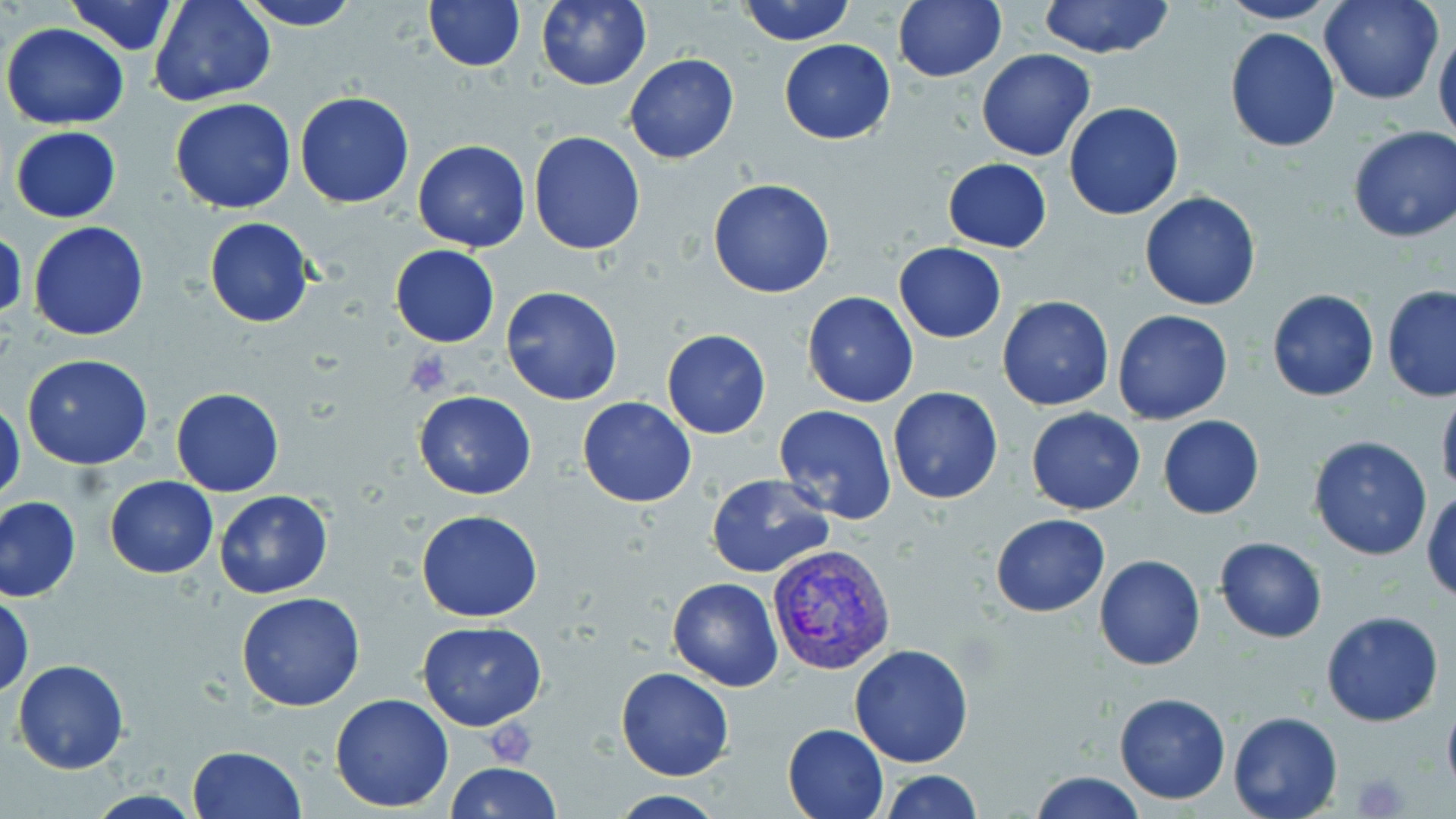

Approximate bounding boxes as [x1, y1, x2, y2] in pixels. Platelet locations: [402, 349, 454, 398], [483, 718, 540, 765], [1353, 772, 1410, 818]. Plasmodium vivax-infected red blood cell locations: [767, 543, 897, 676]. Uninfected red blood cell locations: [64, 0, 182, 55], [149, 0, 275, 107], [236, 0, 362, 31], [424, 0, 525, 71], [535, 0, 651, 90], [738, 0, 856, 45], [894, 0, 1007, 84], [1038, 0, 1175, 58], [1319, 0, 1442, 105], [1216, 1, 1342, 26], [3, 23, 129, 129], [1224, 27, 1340, 153], [1433, 27, 1456, 155], [778, 39, 896, 145], [976, 48, 1096, 161], [624, 52, 739, 165], [1005, 71, 1141, 189], [295, 92, 414, 209], [169, 97, 297, 214], [1064, 101, 1185, 220], [10, 126, 122, 222], [1347, 127, 1456, 243], [529, 131, 645, 255], [412, 139, 531, 252], [942, 159, 1053, 252], [707, 177, 837, 299], [1139, 191, 1262, 311], [204, 216, 314, 328], [27, 220, 150, 341], [1, 226, 26, 327], [894, 243, 1006, 343], [389, 245, 500, 347], [501, 286, 622, 405], [1381, 286, 1456, 403], [1267, 289, 1379, 401], [802, 291, 918, 408], [997, 294, 1114, 411], [1112, 309, 1232, 424], [661, 327, 771, 439], [22, 354, 153, 470], [888, 386, 1004, 503], [1436, 386, 1456, 500], [170, 387, 285, 497], [413, 388, 536, 499], [577, 396, 698, 507], [0, 397, 26, 507], [773, 405, 897, 524], [1026, 408, 1146, 515], [1157, 415, 1265, 519], [1308, 435, 1432, 561], [705, 473, 836, 577], [104, 476, 218, 579], [1423, 489, 1456, 601], [213, 491, 335, 600], [0, 496, 81, 601], [416, 510, 544, 622], [990, 513, 1110, 617], [1214, 537, 1326, 642], [1094, 554, 1205, 671], [666, 577, 782, 690], [0, 592, 34, 700], [237, 592, 366, 711], [1320, 610, 1445, 727], [417, 620, 547, 730], [849, 643, 976, 767], [12, 659, 128, 773], [617, 667, 736, 781], [1113, 691, 1231, 805], [330, 693, 455, 811], [1441, 703, 1456, 794], [1227, 709, 1342, 818], [783, 723, 888, 818], [186, 745, 306, 818], [445, 761, 563, 818], [879, 770, 983, 818], [1030, 770, 1145, 819], [609, 790, 730, 817]. Slide-level diagnosis: Plasmodium vivax. One field of a larger specimen. Thin blood smear. May-Grünwald-Giemsa-stained preparation. Light microscopy. Image is 1456×819 pixels. Captured at 1000x magnification.